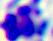

Summary:
  - Identification: white blood cell
  - Modality: photomicrograph
  - Magnification: 400x